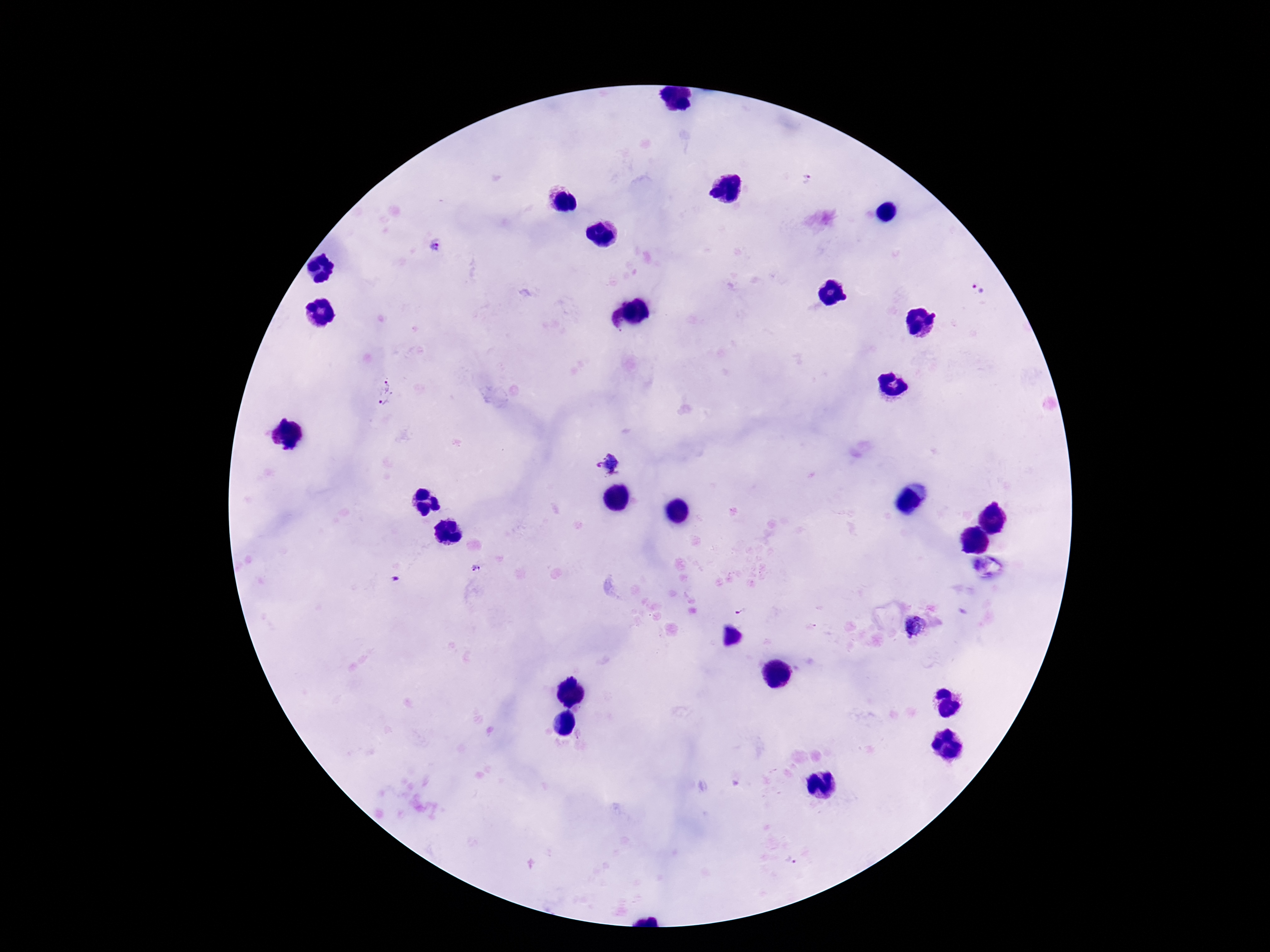
Approximate centers as [x, y] in pixels. Plasmodium parasite locations: [808, 180], [434, 248], [979, 289], [384, 392], [610, 466], [475, 567], [394, 579], [741, 610], [917, 626], [792, 861]. Giemsa stain. 100x magnification. Thick blood film. Smartphone photograph taken through the microscope eyepiece. One field from this slide. Image is 1270×952 pixels. Patient malaria status: infected.